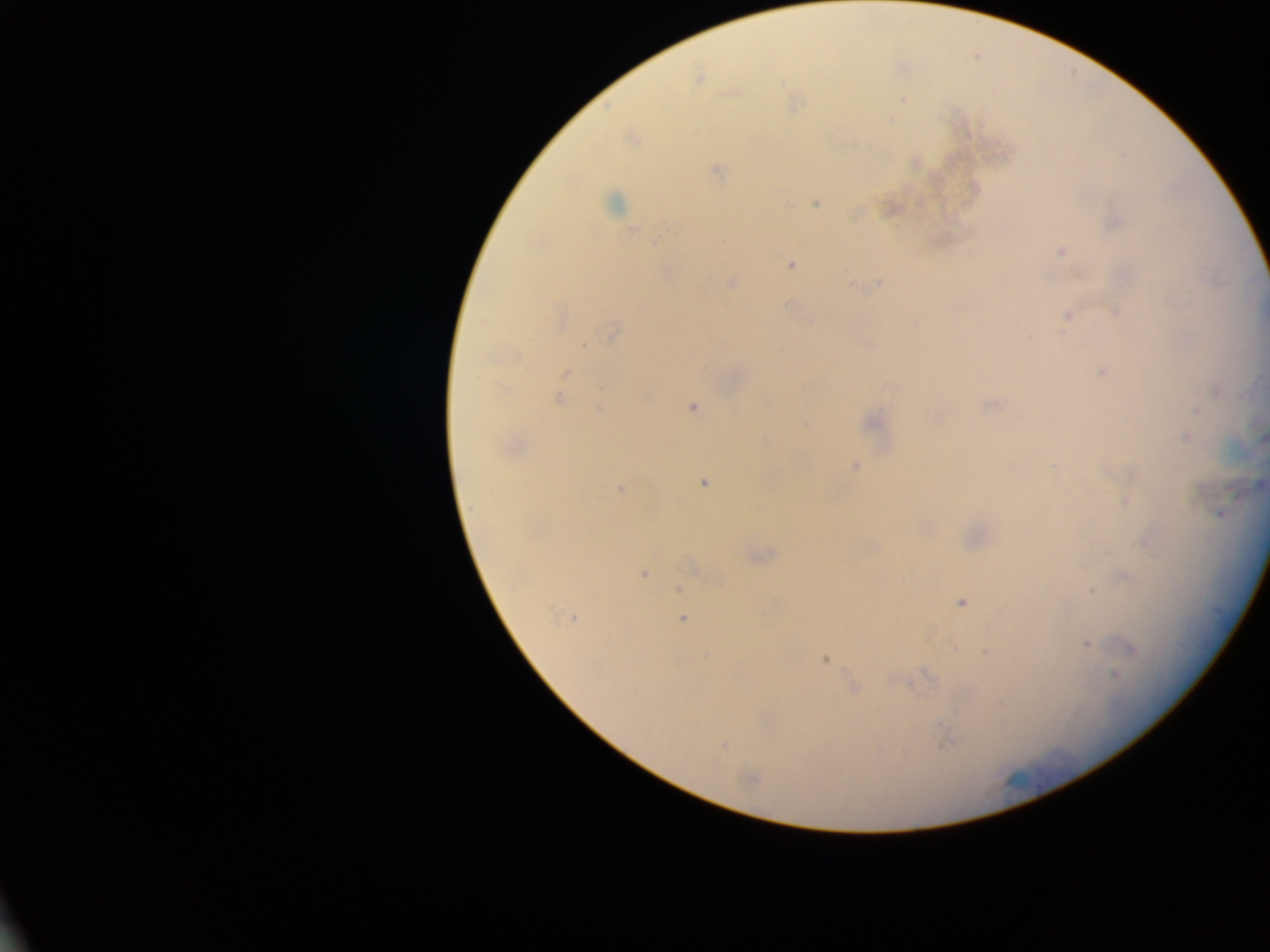
Approximate centers as {x, y} in pixels.
Summary:
  - Plasmodium parasite locations: {699, 79}, {902, 99}, {891, 119}, {633, 140}, {716, 170}, {613, 204}, {816, 204}, {667, 226}, {1060, 252}, {791, 264}, {732, 282}, {878, 283}, {1116, 311}, {1067, 315}, {613, 335}, {1101, 371}, {566, 372}, {505, 389}, {1216, 391}, {558, 400}, {990, 405}, {692, 406}, {599, 409}, {1196, 411}, {1186, 437}, {1261, 437}, {1054, 466}, {855, 467}, {704, 483}, {1261, 484}, {621, 490}, {1220, 513}, {643, 574}, {1125, 578}, {679, 588}, {961, 603}, {572, 618}, {683, 619}, {1087, 643}, {1131, 650}, {986, 652}, {825, 659}, {1114, 675}, {853, 688}, {944, 737}, {724, 745}, {749, 778}
  - Capture: mobile-phone photograph through a microscope
  - Country: Ghana
  - Preparation: thick blood smear
  - Field of view: single
  - Image size: 1270×952 pixels